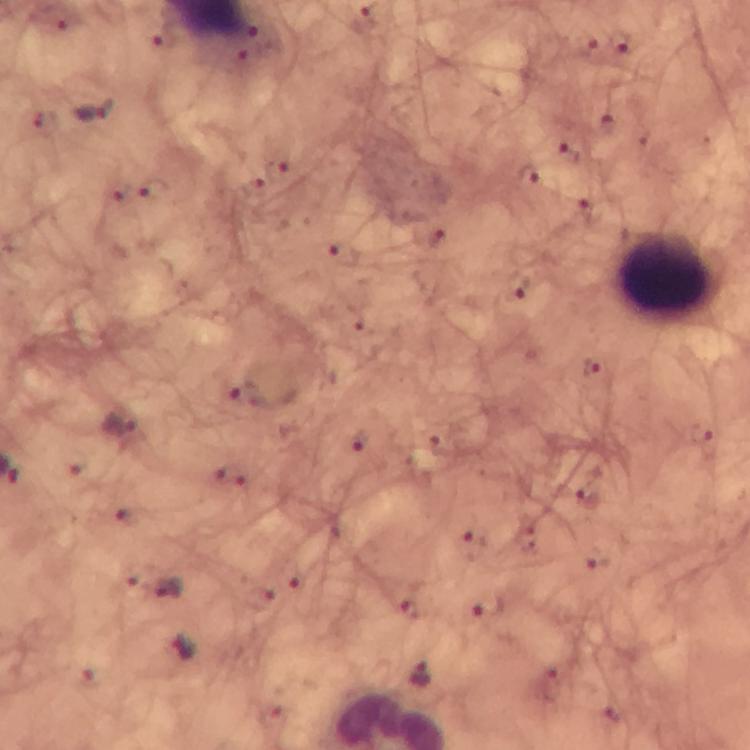

Approximate centers as {x, y} in pixels. Leukocyte locations: {665, 274}. Malaria parasite locations: {365, 22}, {619, 41}, {92, 108}, {566, 151}, {277, 172}, {528, 175}, {257, 188}, {436, 238}, {343, 258}, {516, 288}, {594, 368}, {246, 394}, {120, 425}, {700, 433}, {361, 442}, {230, 475}, {586, 497}, {128, 515}, {473, 546}, {600, 562}, {166, 588}, {488, 605}, {411, 609}, {183, 647}, {417, 673}. Giemsa-stained preparation. A crop from one field of view. Thick blood film. Photographed with a smartphone mounted on the microscope. Immersion oil was used. At 100x magnification. From a diagnostic examination for malaria. Image is 750×750 pixels.